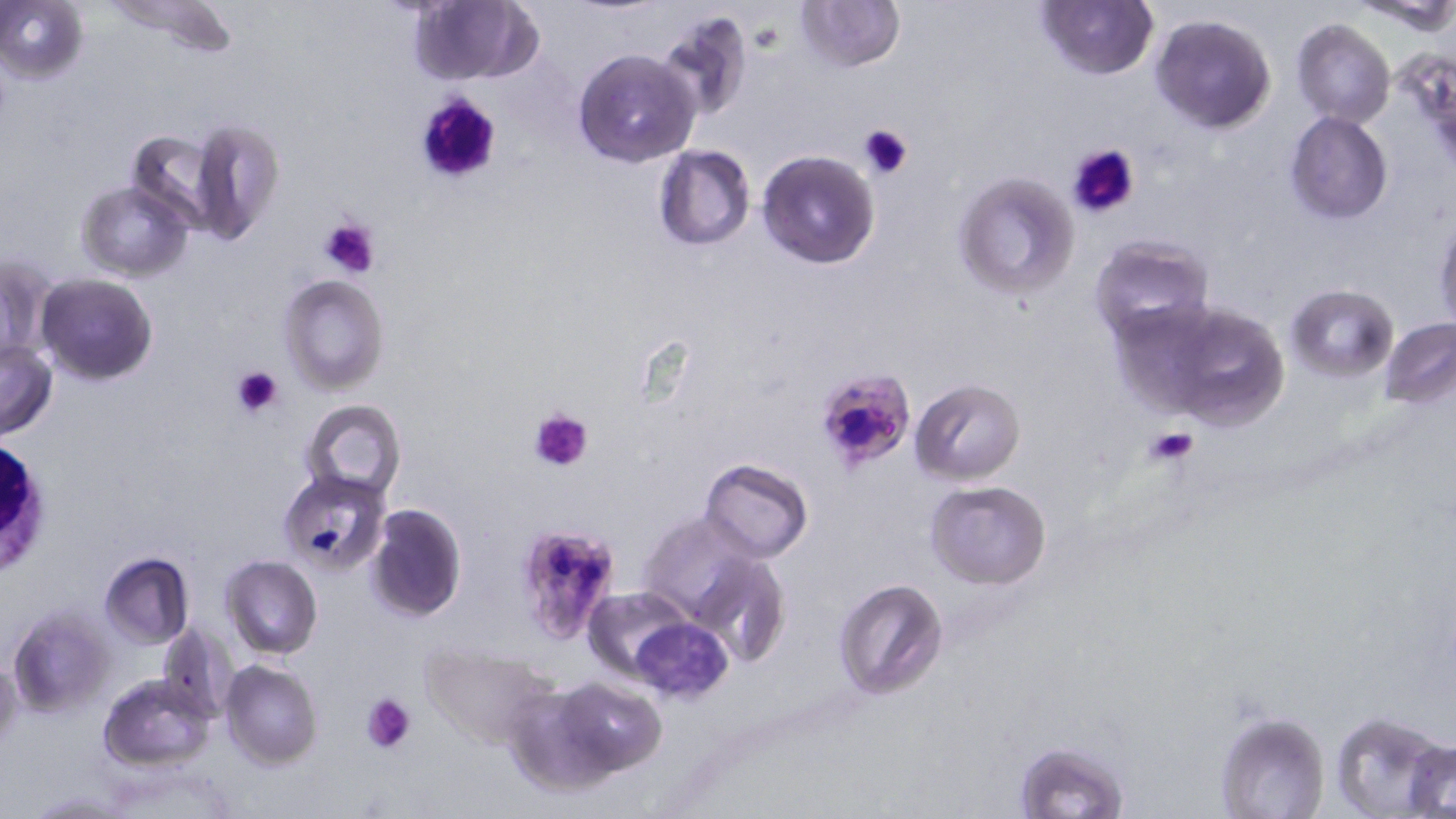

{
  "slide_level_diagnosis": "Plasmodium falciparum",
  "white_blood_cell_locations": "approximate bounding boxes as named x1/y1/x2/y2 corners in pixels: (x1=0, y1=436, x2=48, y2=581)",
  "platelet_locations": "approximate bounding boxes as named x1/y1/x2/y2 corners in pixels: (x1=412, y1=88, x2=504, y2=188), (x1=858, y1=121, x2=913, y2=179), (x1=1066, y1=144, x2=1142, y2=219), (x1=318, y1=216, x2=380, y2=279), (x1=232, y1=364, x2=285, y2=418), (x1=530, y1=408, x2=593, y2=473), (x1=1143, y1=424, x2=1200, y2=468), (x1=360, y1=693, x2=415, y2=754)",
  "modality": "light microscopy",
  "field_of_view": "single",
  "magnification": "1000x",
  "image_size": "1456×819 pixels",
  "stain": "May-Grünwald-Giemsa",
  "uninfected_red_blood_cell_locations": "approximate bounding boxes as named x1/y1/x2/y2 corners in pixels: (x1=106, y1=0, x2=238, y2=50), (x1=795, y1=0, x2=904, y2=73), (x1=0, y1=1, x2=88, y2=84), (x1=407, y1=1, x2=542, y2=87), (x1=1036, y1=1, x2=1157, y2=80), (x1=1355, y1=1, x2=1456, y2=33), (x1=655, y1=8, x2=754, y2=120), (x1=1149, y1=13, x2=1276, y2=132), (x1=1290, y1=19, x2=1395, y2=128), (x1=574, y1=49, x2=700, y2=167), (x1=1286, y1=111, x2=1393, y2=223), (x1=188, y1=117, x2=285, y2=243), (x1=126, y1=129, x2=221, y2=234), (x1=652, y1=144, x2=755, y2=251), (x1=757, y1=149, x2=881, y2=269), (x1=952, y1=171, x2=1079, y2=300), (x1=77, y1=180, x2=195, y2=281), (x1=1435, y1=219, x2=1456, y2=331), (x1=1090, y1=237, x2=1214, y2=345), (x1=0, y1=255, x2=56, y2=364), (x1=37, y1=273, x2=158, y2=386), (x1=280, y1=274, x2=389, y2=393), (x1=1287, y1=285, x2=1396, y2=380), (x1=1156, y1=301, x2=1294, y2=433), (x1=1379, y1=319, x2=1456, y2=409), (x1=0, y1=341, x2=57, y2=441), (x1=910, y1=379, x2=1025, y2=483), (x1=301, y1=399, x2=407, y2=502), (x1=700, y1=458, x2=813, y2=562), (x1=278, y1=471, x2=393, y2=579), (x1=924, y1=479, x2=1052, y2=588), (x1=364, y1=503, x2=466, y2=620), (x1=637, y1=513, x2=766, y2=630), (x1=99, y1=553, x2=194, y2=648), (x1=686, y1=553, x2=789, y2=669), (x1=220, y1=555, x2=323, y2=659), (x1=832, y1=577, x2=949, y2=701), (x1=583, y1=586, x2=695, y2=681), (x1=9, y1=605, x2=115, y2=717), (x1=631, y1=617, x2=733, y2=703), (x1=156, y1=622, x2=236, y2=722), (x1=421, y1=643, x2=559, y2=750), (x1=0, y1=654, x2=23, y2=758), (x1=220, y1=659, x2=323, y2=769), (x1=99, y1=673, x2=216, y2=769), (x1=553, y1=678, x2=666, y2=775), (x1=499, y1=684, x2=625, y2=797), (x1=1212, y1=710, x2=1330, y2=819), (x1=1330, y1=710, x2=1453, y2=818), (x1=1015, y1=740, x2=1128, y2=816), (x1=1408, y1=740, x2=1456, y2=818)",
  "preparation": "thin blood smear",
  "plasmodium_falciparum_infected_red_blood_cell_locations": "approximate bounding boxes as named x1/y1/x2/y2 corners in pixels: (x1=812, y1=368, x2=919, y2=474), (x1=516, y1=518, x2=623, y2=641)"
}